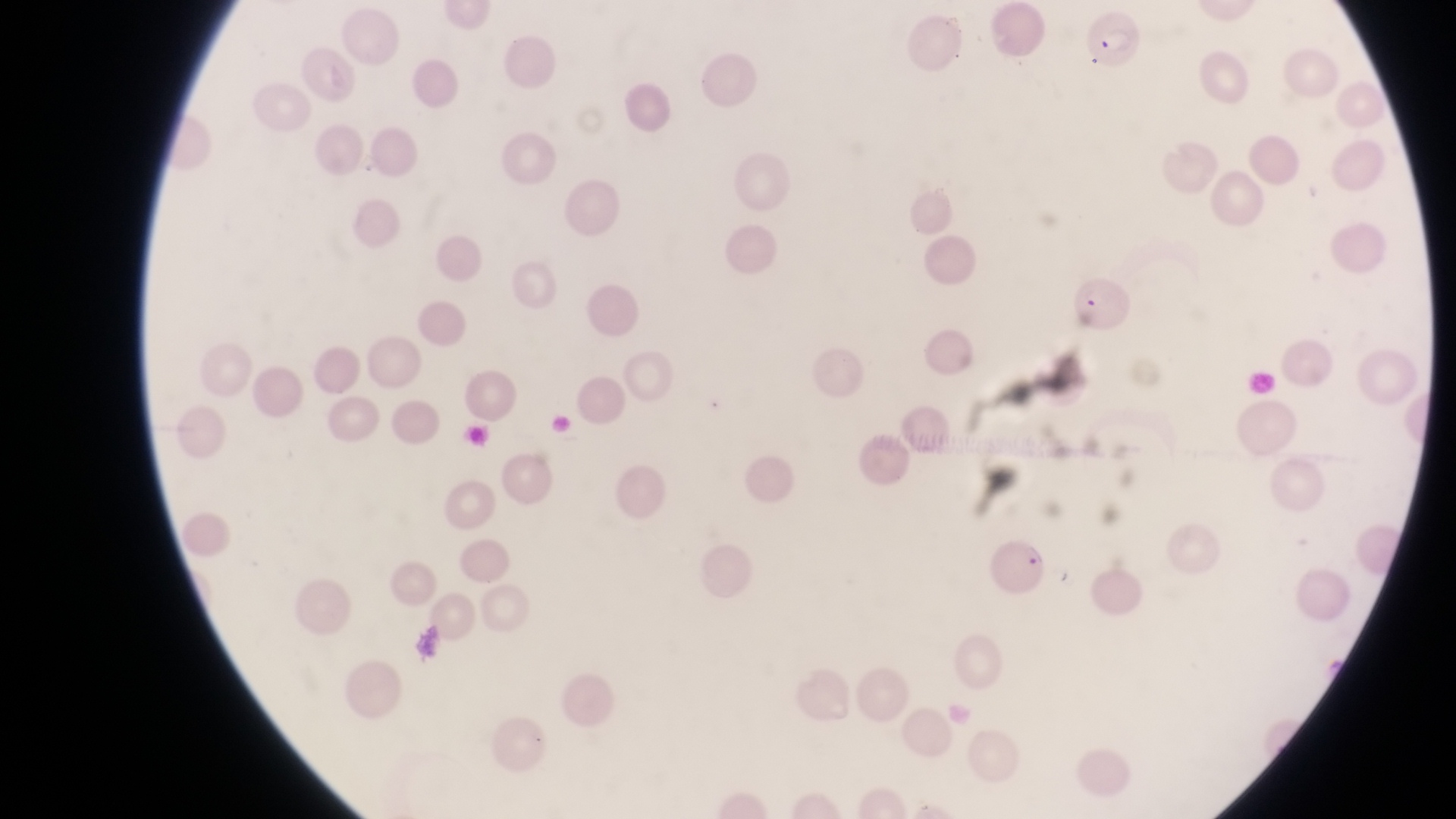

Approximate bounding boxes as {left, top, right, bottom} in pixels.
Summary:
  - Parasitised red blood cell locations: {1067, 274, 1130, 334}, {980, 534, 1053, 597}
  - Image size: 1456×819 pixels
  - Magnification: 1000x
  - Country: Uganda
  - Field of view: single
  - Preparation: thin blood film
  - Capture: smartphone photograph through the eyepiece of an Olympus CX-23 microscope